State the preparation type.
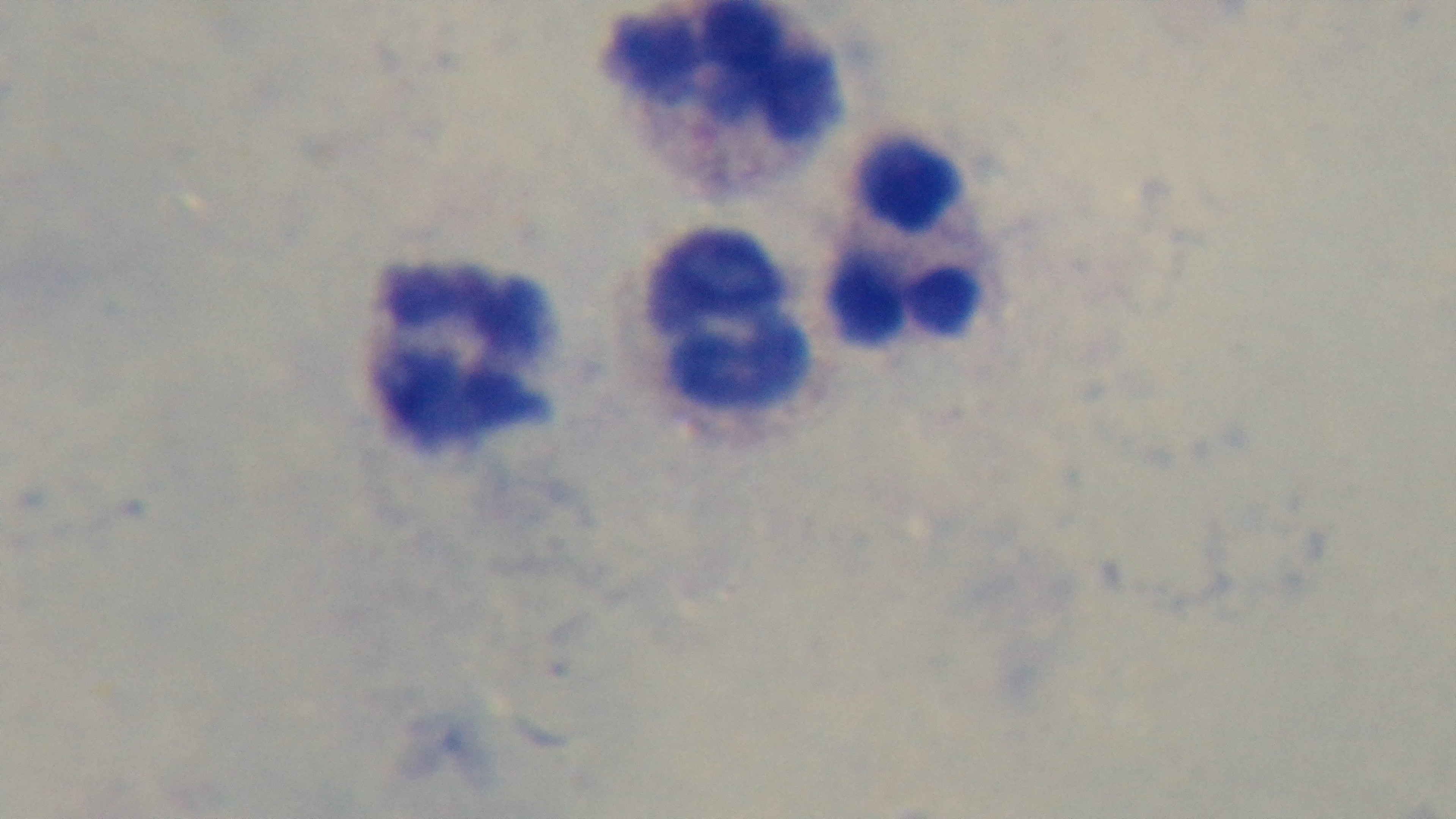
It is a thick blood film.

objective = 100x oil immersion
field of view = one from the slide
malaria status = negative
capture = mounted 4K digital camera
stain = Giemsa
modality = light microscopy